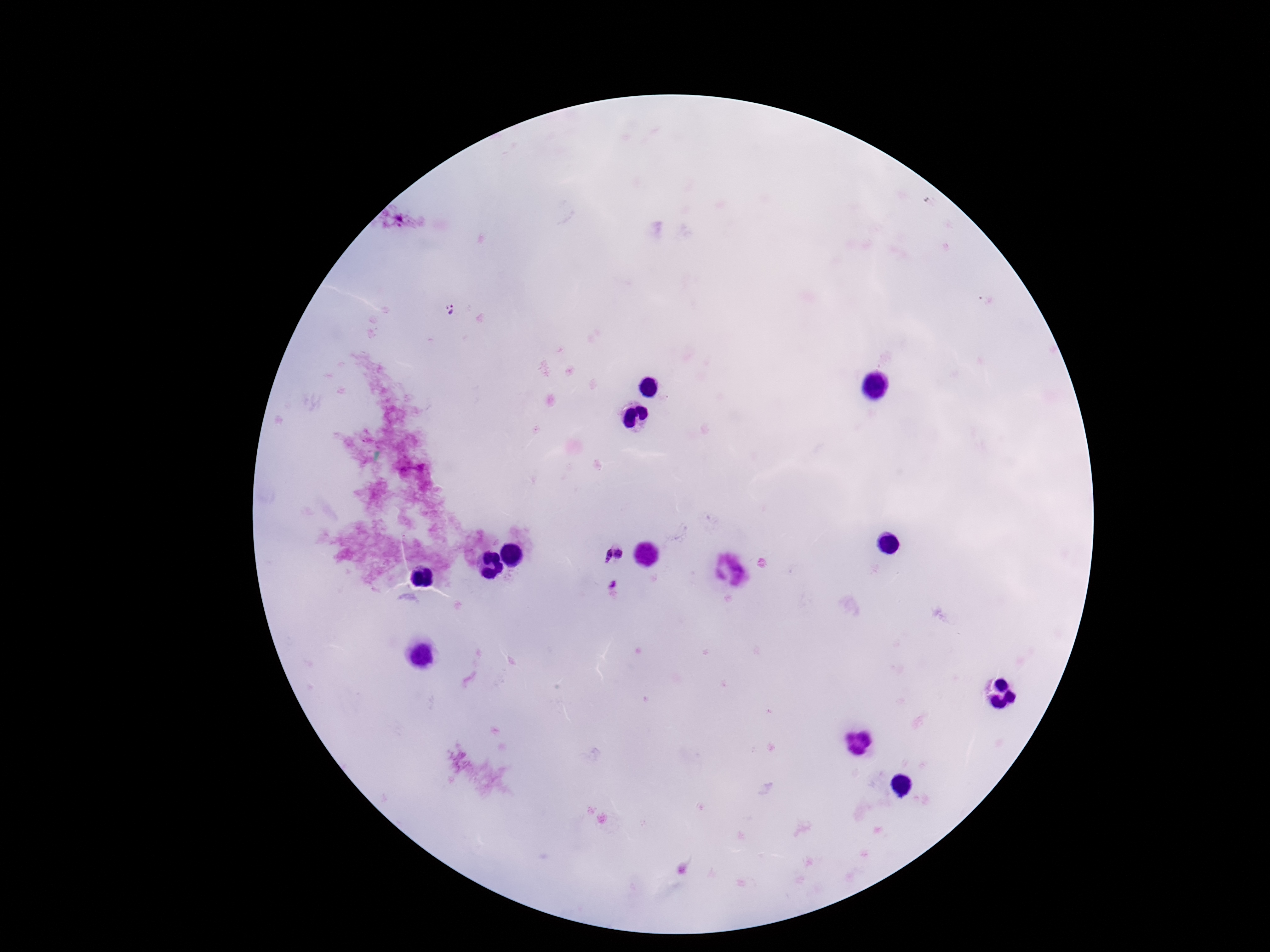

Approximate centers as (x, y) in pixels. Plasmodium parasite locations: (449, 310), (620, 554), (605, 555), (614, 588). Smartphone photograph taken through the microscope eyepiece. Image is 1270×952 pixels. Giemsa stain. Thick blood film. Patient malaria status: infected. One field from this slide. 100x magnification.